Outline each blood parasite and name the species.
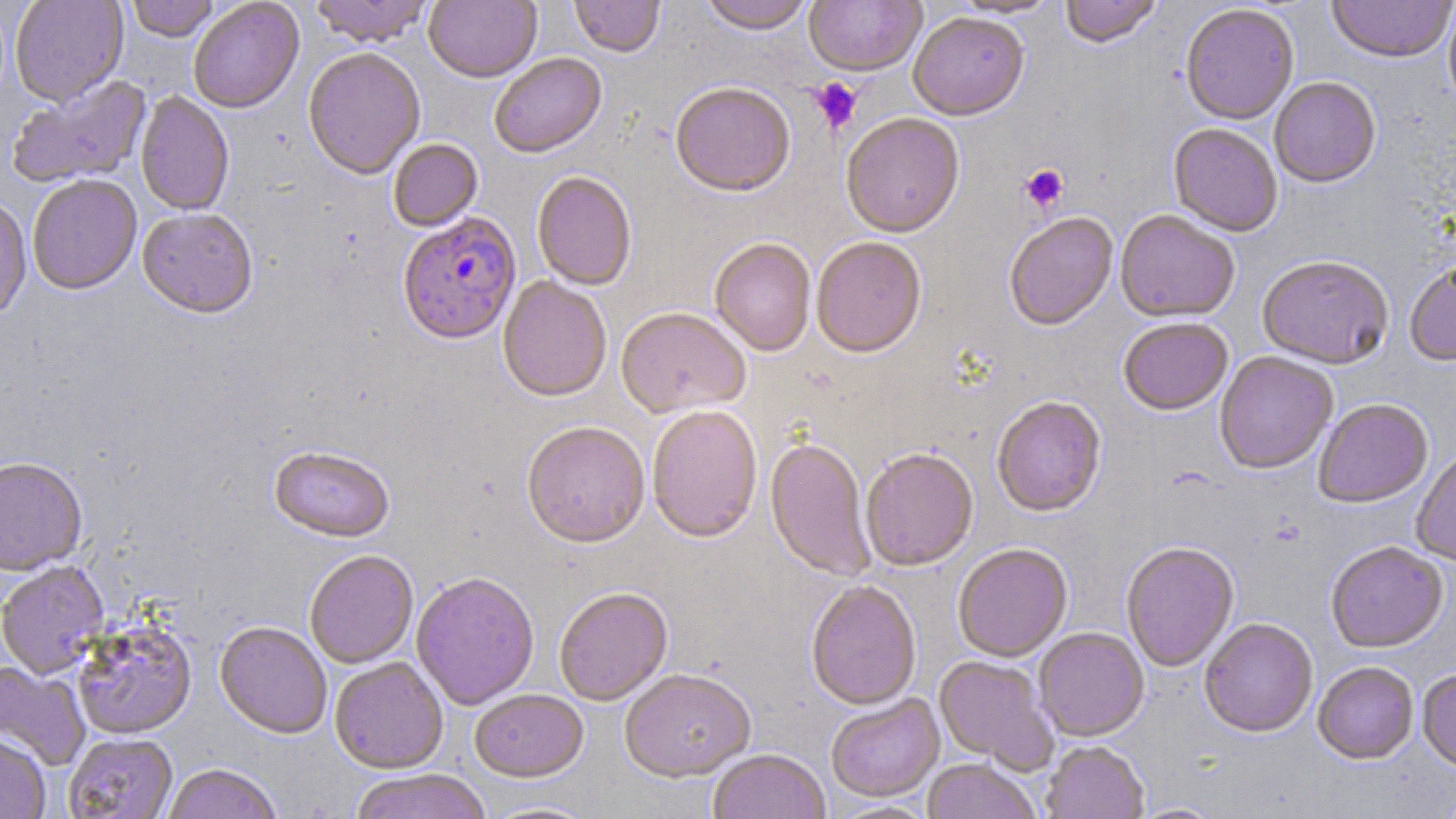

Approximate bounding boxes as (x1,y1)-(x2,y2) corner pairs in pixels.
Plasmodium falciparum-infected red blood cells: (397,213)-(521,348).
No Plasmodium ovale, Plasmodium malariae, Plasmodium vivax, Babesia divergens, or Trypanosoma brucei observed.

Uninfected red blood cell locations: (10,0)-(128,107), (126,0)-(220,43), (308,0)-(435,49), (424,0)-(542,86), (569,0)-(665,59), (699,0)-(815,36), (949,0)-(1063,19), (1059,0)-(1164,50), (1325,0)-(1456,65), (188,1)-(305,115), (803,1)-(927,79), (1443,2)-(1456,114), (1180,4)-(1299,127), (908,14)-(1029,123), (303,50)-(425,183), (490,54)-(607,161), (6,76)-(153,190), (1269,78)-(1382,190), (670,85)-(796,199), (134,92)-(234,217), (841,115)-(965,241), (1168,124)-(1283,238), (388,140)-(484,233), (532,172)-(637,292), (27,176)-(142,297), (0,195)-(32,324), (137,210)-(258,322), (1115,212)-(1239,325), (1005,215)-(1118,333), (811,239)-(927,361), (710,240)-(816,358), (1257,258)-(1394,371), (1404,263)-(1456,369), (497,278)-(611,405), (615,310)-(751,420), (1118,319)-(1234,418), (1214,352)-(1338,476), (992,398)-(1106,519), (1314,400)-(1433,510), (646,408)-(762,546), (521,424)-(650,551), (764,438)-(876,584), (268,448)-(395,546), (861,450)-(978,572), (1412,451)-(1456,567), (0,459)-(89,577), (1121,543)-(1239,673), (1325,543)-(1448,654), (953,545)-(1073,663), (304,552)-(418,669), (0,562)-(109,679), (411,574)-(539,711), (806,582)-(922,713), (554,589)-(673,706), (72,619)-(198,741), (1199,620)-(1318,739), (214,623)-(332,741), (1033,629)-(1149,742), (934,656)-(1058,773), (330,658)-(448,775), (0,661)-(91,772), (1312,663)-(1419,766), (1417,670)-(1456,775), (620,672)-(757,784), (469,691)-(589,785), (826,696)-(945,804), (64,733)-(178,818), (0,734)-(51,819), (1041,742)-(1149,819), (707,751)-(830,819), (922,760)-(1039,819), (163,764)-(283,819), (348,771)-(492,819), (1130,803)-(1225,819). Platelet locations: (810,78)-(863,133), (1019,164)-(1069,214). Slide-level diagnosis: Plasmodium falciparum. May-Grünwald-Giemsa-stained preparation. Single field of view. Light microscopy. Image is 1456×819 pixels. Captured at 1000x magnification. Thin blood smear.